Name the parasite shown.
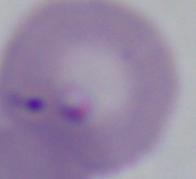
This is Babesia.

Summary:
  - Magnification: 1000x
  - Modality: photomicrograph